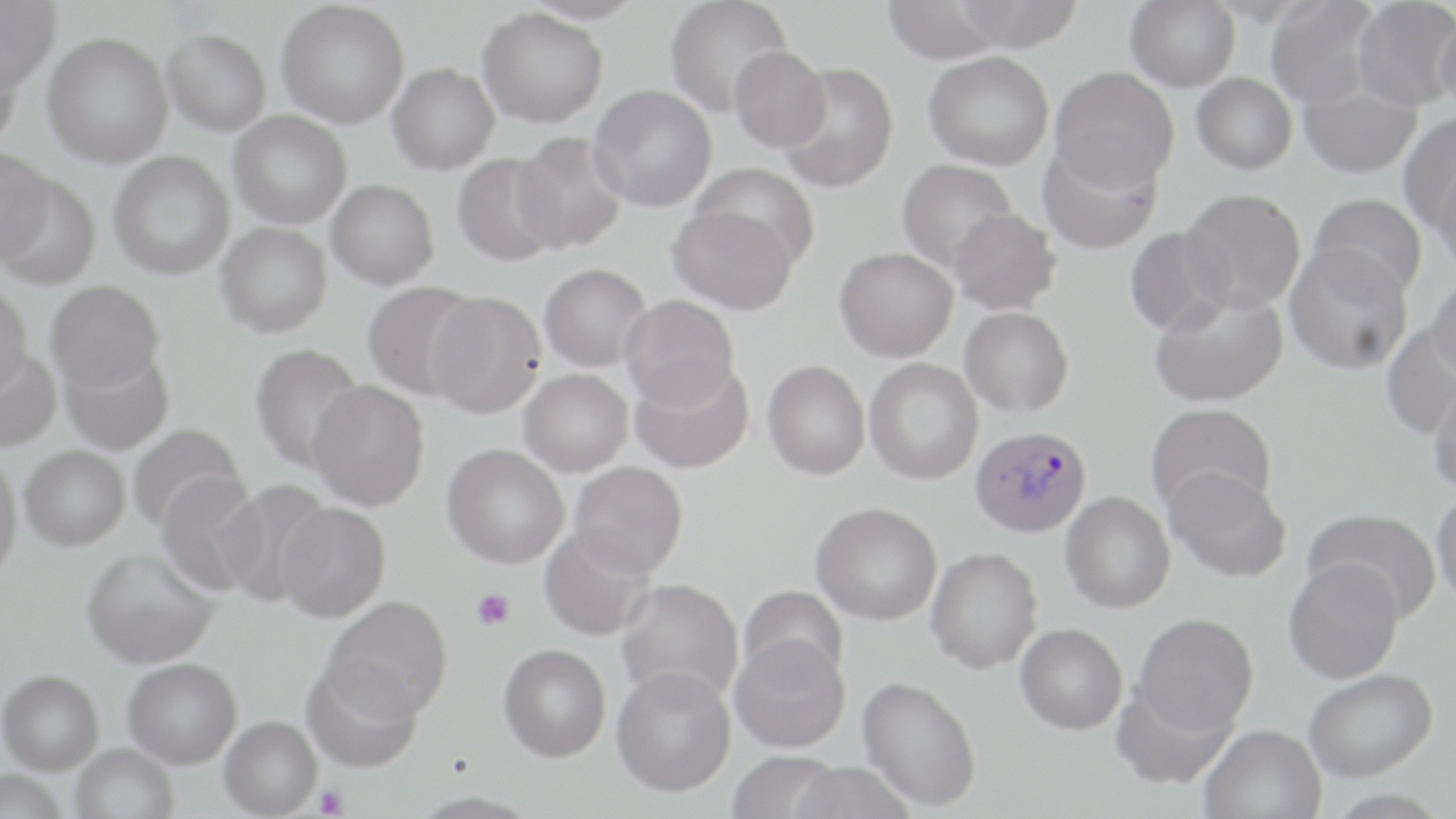
Approximate bounding boxes as (x1,y1)-(x2,y2) corner pairs in pixels. Platelet locations: (472,588)-(515,630), (316,786)-(349,818). Plasmodium vivax-infected red blood cell locations: (970,425)-(1092,538). Uninfected red blood cell locations: (0,0)-(60,92), (520,0)-(644,25), (664,0)-(793,117), (880,0)-(1009,65), (952,0)-(1084,53), (1125,0)-(1240,91), (1265,0)-(1380,108), (1351,0)-(1456,112), (276,1)-(409,129), (477,7)-(608,128), (1435,12)-(1456,117), (161,29)-(271,136), (41,31)-(173,168), (0,39)-(25,150), (729,45)-(832,152), (924,52)-(1054,170), (387,63)-(499,175), (777,63)-(898,190), (1050,67)-(1179,191), (1191,73)-(1297,174), (1299,83)-(1420,178), (588,85)-(717,212), (228,110)-(352,229), (1397,113)-(1456,232), (510,132)-(628,254), (1037,139)-(1163,256), (0,145)-(53,265), (108,150)-(235,280), (452,153)-(563,267), (897,159)-(1018,273), (690,161)-(821,269), (1432,166)-(1456,274), (0,174)-(101,291), (326,179)-(439,289), (1179,188)-(1305,315), (1309,193)-(1428,300), (667,205)-(798,315), (948,207)-(1061,315), (216,221)-(332,337), (1124,227)-(1229,337), (1284,244)-(1414,374), (834,247)-(958,362), (538,263)-(652,372), (1427,271)-(1456,385), (45,280)-(164,392), (361,280)-(482,399), (0,283)-(32,399), (1149,288)-(1288,407), (425,290)-(547,418), (619,294)-(739,410), (960,306)-(1073,417), (1381,322)-(1456,440), (250,343)-(365,472), (0,347)-(62,453), (60,347)-(175,455), (864,358)-(983,485), (629,360)-(753,474), (762,360)-(870,480), (519,368)-(633,476), (1428,374)-(1456,494), (307,380)-(429,511), (1146,403)-(1277,518), (126,424)-(246,532), (441,443)-(569,568), (19,445)-(130,550), (0,452)-(23,582), (569,461)-(688,578), (1164,465)-(1291,582), (156,472)-(265,595), (215,479)-(332,607), (1431,488)-(1456,608), (1060,492)-(1175,613), (276,502)-(390,622), (811,502)-(942,625), (1304,508)-(1442,623), (539,526)-(655,641), (81,547)-(219,668), (925,547)-(1043,674), (1283,558)-(1404,684), (616,578)-(743,705), (738,586)-(848,687), (321,595)-(453,722), (1133,613)-(1259,735), (1015,623)-(1127,734), (730,634)-(850,753), (498,643)-(611,762), (122,657)-(242,769), (301,659)-(424,773), (611,665)-(736,796), (1304,668)-(1438,781), (0,669)-(103,774), (857,675)-(982,811), (1111,681)-(1238,789), (218,716)-(322,818), (1199,723)-(1326,819), (70,744)-(178,819), (725,750)-(843,819), (787,760)-(916,819). Slide-level diagnosis: Plasmodium vivax. Image is 1456×819 pixels. Thin blood film. May-Grünwald-Giemsa-stained preparation. One field of a larger specimen. Captured at 1000x magnification. Optical microscopy.